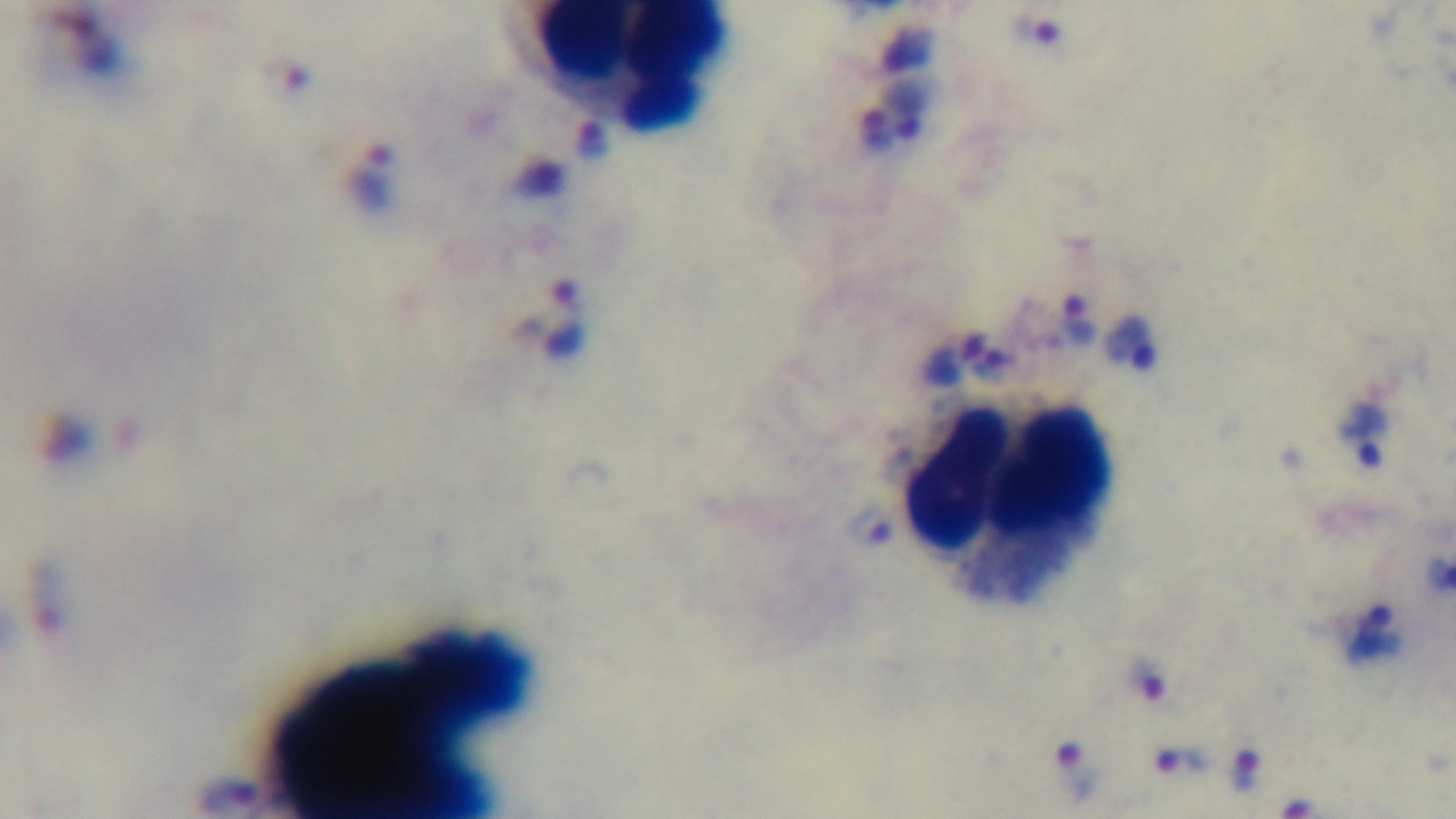
{
  "preparation": "thick blood film",
  "capture": "mounted 4K digital camera",
  "modality": "light microscopy",
  "stain": "Giemsa",
  "field_of_view": "one from the slide",
  "malaria_status": "infected",
  "objective": "100x oil immersion"
}